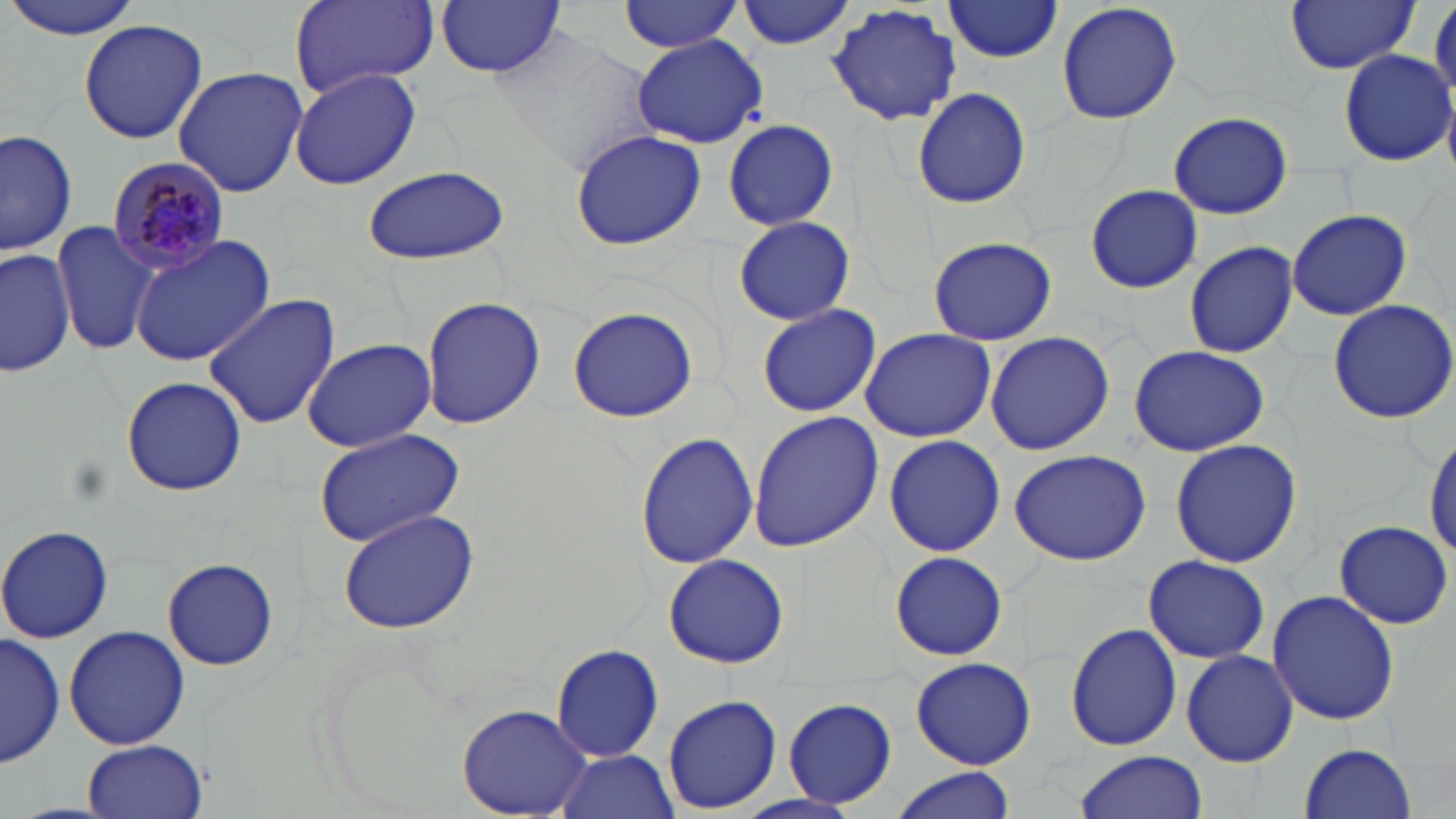
slide-level diagnosis = Plasmodium malariae
uninfected red blood cell locations = approximate bounding boxes as [x1, y1, x2, y2] in pixels: [1, 0, 148, 39], [735, 0, 856, 51], [1056, 0, 1182, 127], [1286, 0, 1420, 74], [290, 1, 439, 101], [436, 1, 565, 76], [619, 1, 743, 53], [942, 1, 1064, 63], [1430, 1, 1456, 105], [827, 4, 962, 127], [77, 21, 210, 145], [488, 26, 659, 174], [632, 36, 771, 148], [1338, 49, 1454, 166], [172, 66, 308, 197], [289, 66, 421, 192], [912, 86, 1031, 210], [1168, 110, 1293, 220], [720, 120, 842, 231], [0, 126, 75, 255], [569, 130, 705, 248], [360, 165, 511, 265], [1085, 185, 1203, 292], [1285, 208, 1412, 321], [733, 216, 854, 324], [50, 220, 160, 354], [130, 235, 273, 367], [928, 236, 1056, 345], [1183, 241, 1299, 358], [0, 243, 74, 378], [203, 294, 340, 431], [422, 297, 545, 430], [1326, 299, 1456, 425], [756, 303, 881, 418], [566, 306, 699, 423], [860, 327, 996, 443], [984, 330, 1115, 456], [301, 338, 436, 452], [1128, 343, 1271, 457], [121, 377, 247, 496], [748, 411, 883, 550], [313, 427, 467, 548], [1425, 428, 1456, 562], [634, 431, 760, 570], [883, 432, 1005, 557], [1169, 437, 1303, 569], [1008, 447, 1152, 566], [335, 505, 480, 634], [1335, 520, 1454, 630], [0, 524, 114, 644], [889, 550, 1008, 662], [663, 553, 789, 670], [1142, 554, 1270, 664], [163, 558, 278, 672], [1266, 589, 1400, 726], [1066, 623, 1183, 751], [64, 625, 190, 751], [1, 631, 64, 769], [552, 645, 663, 763], [1180, 649, 1299, 767], [909, 656, 1036, 769], [662, 695, 781, 814], [782, 697, 897, 809], [458, 705, 591, 816], [83, 738, 207, 819], [1298, 742, 1417, 816], [551, 749, 680, 819], [1072, 751, 1207, 819], [885, 767, 1020, 819]
field of view = one of a larger specimen
stain = May-Grünwald-Giemsa
modality = optical microscopy
preparation = thin blood smear
magnification = 1000x
Plasmodium malariae-infected red blood cell locations = approximate bounding boxes as [x1, y1, x2, y2] in pixels: [103, 154, 233, 277]
image size = 1456×819 pixels